Give the extent of all uninfected red blood cells.
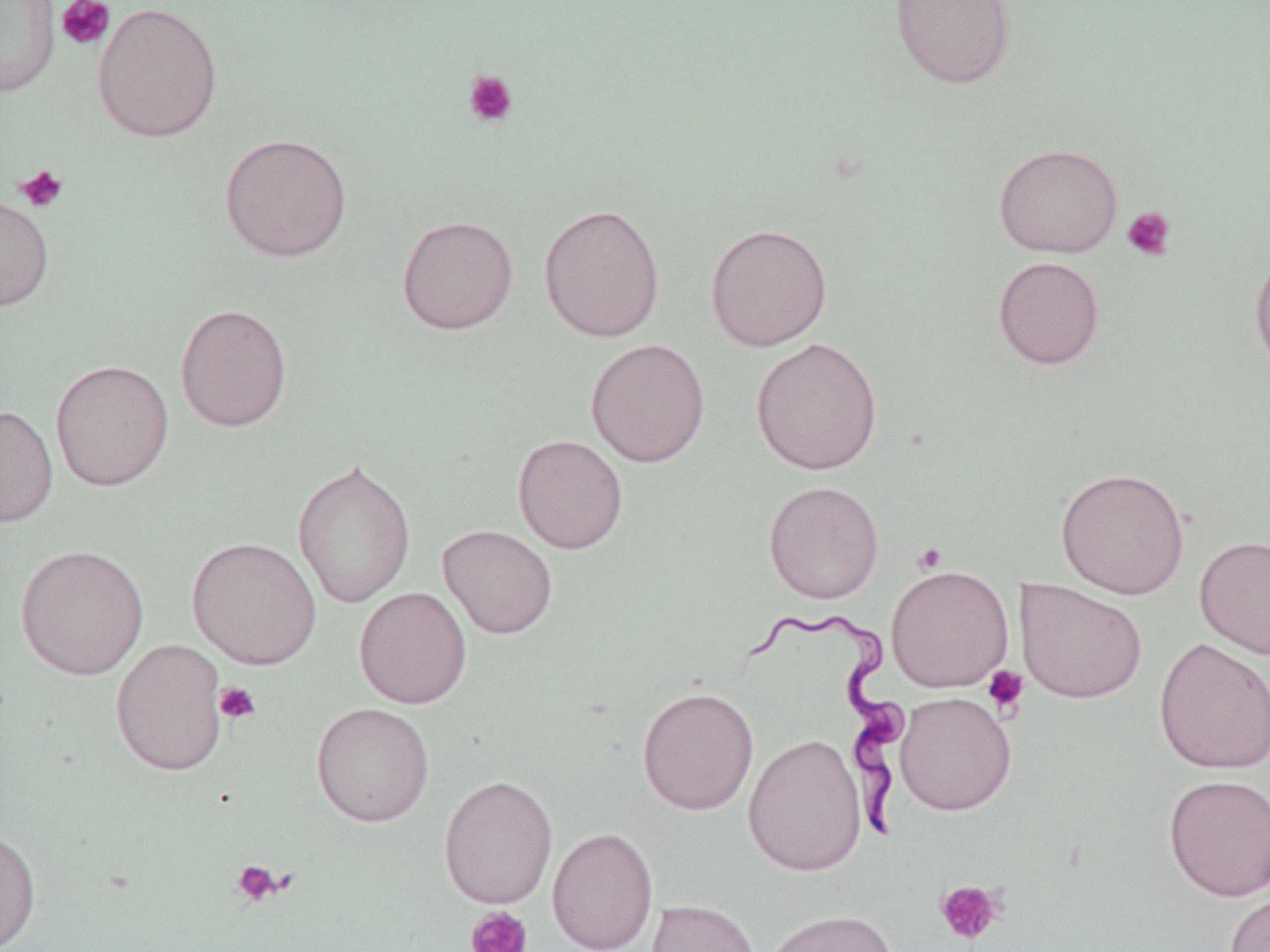
Approximate bounding boxes as named x1/y1/x2/y2 corners in pixels.
Uninfected red blood cells: (x1=0, y1=0, x2=61, y2=97), (x1=890, y1=0, x2=1016, y2=90), (x1=92, y1=1, x2=223, y2=143), (x1=219, y1=132, x2=353, y2=262), (x1=993, y1=142, x2=1123, y2=258), (x1=0, y1=193, x2=54, y2=311), (x1=538, y1=203, x2=666, y2=342), (x1=396, y1=214, x2=519, y2=335), (x1=705, y1=222, x2=833, y2=351), (x1=1249, y1=248, x2=1270, y2=379), (x1=992, y1=256, x2=1105, y2=370), (x1=174, y1=302, x2=293, y2=432), (x1=749, y1=336, x2=883, y2=476), (x1=585, y1=338, x2=711, y2=468), (x1=50, y1=359, x2=174, y2=492), (x1=0, y1=404, x2=58, y2=527), (x1=512, y1=434, x2=629, y2=554), (x1=291, y1=457, x2=416, y2=609), (x1=1055, y1=467, x2=1190, y2=600), (x1=763, y1=480, x2=885, y2=604), (x1=437, y1=523, x2=558, y2=639), (x1=187, y1=535, x2=322, y2=670), (x1=1194, y1=535, x2=1270, y2=659), (x1=15, y1=544, x2=150, y2=681), (x1=885, y1=564, x2=1014, y2=692), (x1=1015, y1=578, x2=1147, y2=705), (x1=353, y1=586, x2=472, y2=709), (x1=1153, y1=636, x2=1270, y2=775), (x1=110, y1=637, x2=229, y2=776), (x1=636, y1=686, x2=759, y2=816), (x1=894, y1=691, x2=1016, y2=816), (x1=311, y1=702, x2=435, y2=827), (x1=742, y1=733, x2=868, y2=877), (x1=1162, y1=773, x2=1270, y2=902), (x1=438, y1=774, x2=559, y2=909), (x1=0, y1=825, x2=42, y2=952), (x1=547, y1=826, x2=659, y2=952), (x1=1223, y1=891, x2=1270, y2=952), (x1=644, y1=899, x2=761, y2=952), (x1=761, y1=908, x2=900, y2=952).

Trypanosoma brucei locations = approximate bounding boxes as named x1/y1/x2/y2 corners in pixels: (x1=738, y1=602, x2=915, y2=847)
slide-level diagnosis = Trypanosoma brucei
platelet locations = approximate bounding boxes as named x1/y1/x2/y2 corners in pixels: (x1=55, y1=0, x2=115, y2=50), (x1=463, y1=70, x2=518, y2=128), (x1=14, y1=164, x2=69, y2=213), (x1=1122, y1=206, x2=1177, y2=261), (x1=911, y1=541, x2=949, y2=573), (x1=982, y1=665, x2=1029, y2=716), (x1=214, y1=681, x2=261, y2=725), (x1=232, y1=858, x2=287, y2=907), (x1=934, y1=879, x2=1006, y2=946), (x1=465, y1=906, x2=533, y2=952)
preparation = thin blood smear
image size = 1270×952 pixels
magnification = 1000x
stain = May-Grünwald-Giemsa
modality = optical microscopy
field of view = one of a larger specimen